Identify the cell.
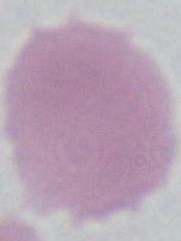
An erythrocyte.

modality = micrograph
magnification = 1000x